Classify this cell by malaria status.
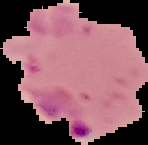
It is parasitized.

image size = 148×145 pixels
preparation = thin blood film
image type = cell region segmented out of the field of view; surrounding area masked to black